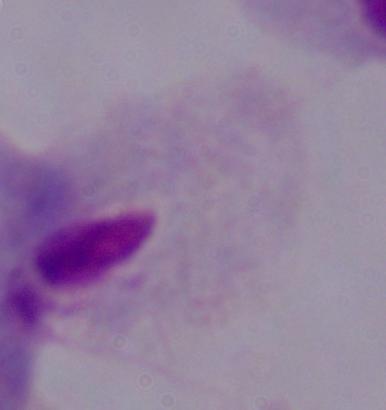

magnification = 1000x
identification = trichomonad
modality = micrograph